Assess this cell for malaria.
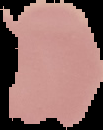

Uninfected.

preparation = thin blood smear
image type = segmented cell region on a black background
image size = 103×130 pixels